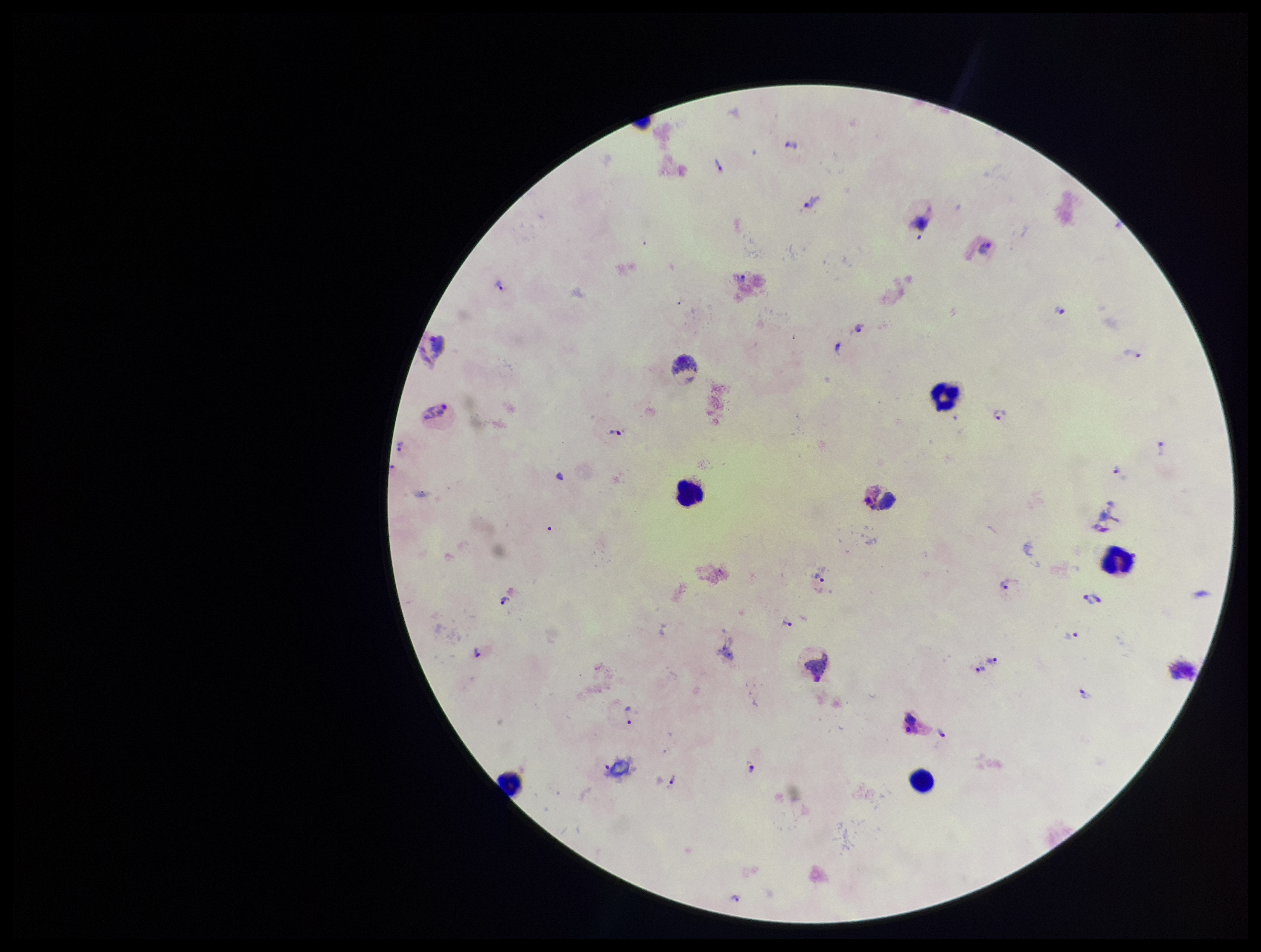
Summary:
  - Field of view: single
  - Image size: 1261×952 pixels
  - Species reported for this patient: Plasmodium vivax
  - Leukocyte count: 5
  - Parasite count: 26
  - Preparation: thick
  - Patient malaria status: positive
  - Stain: Giemsa
  - Plasmodium parasites: identified
  - Capture: smartphone photograph through the microscope eyepiece